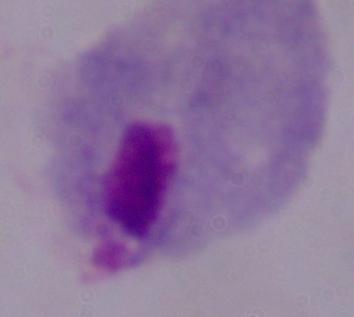
Summary:
  - Magnification: 1000x
  - Identification: trichomonad
  - Modality: photomicrograph